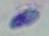

Summary:
  - Modality: micrograph
  - Identification: Toxoplasma gondii
  - Magnification: 1000x